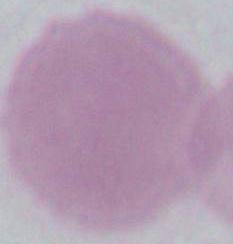
Micrograph. Captured at 1000x magnification. A red blood cell is seen.